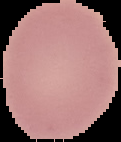

Summary:
  - Image type: cell region segmented out of the field of view; surrounding area masked to black
  - Result: negative for Plasmodium parasites
  - Preparation: thin blood film
  - Image size: 121×142 pixels